Give the extent of all white blood cells.
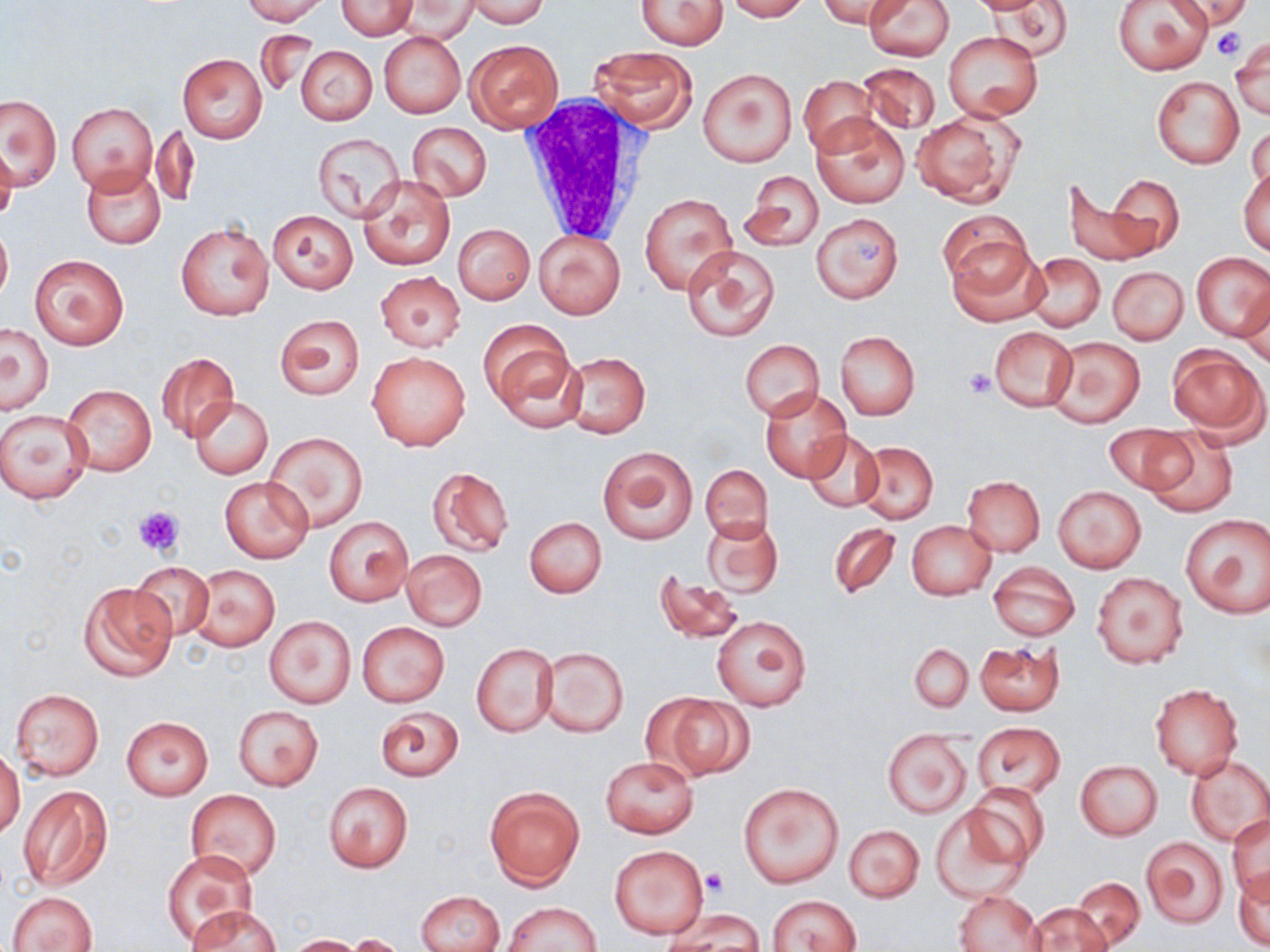

Approximate bounding boxes as named x1/y1/x2/y2 corners in pixels.
White blood cells: (x1=517, y1=93, x2=650, y2=247).

slide-level diagnosis = no evidence of blood parasites
magnification = 1000x
uninfected red blood cell locations = approximate bounding boxes as named x1/y1/x2/y2 corners in pixels: (x1=239, y1=0, x2=329, y2=24), (x1=335, y1=0, x2=417, y2=39), (x1=724, y1=0, x2=809, y2=21), (x1=819, y1=0, x2=906, y2=32), (x1=863, y1=0, x2=954, y2=60), (x1=983, y1=0, x2=1075, y2=60), (x1=1173, y1=0, x2=1250, y2=31), (x1=464, y1=1, x2=552, y2=26), (x1=636, y1=1, x2=729, y2=50), (x1=1112, y1=1, x2=1213, y2=74), (x1=395, y1=2, x2=476, y2=42), (x1=255, y1=31, x2=320, y2=94), (x1=378, y1=31, x2=465, y2=118), (x1=943, y1=31, x2=1043, y2=121), (x1=464, y1=38, x2=564, y2=133), (x1=1231, y1=38, x2=1269, y2=117), (x1=295, y1=45, x2=376, y2=125), (x1=589, y1=46, x2=699, y2=132), (x1=178, y1=53, x2=267, y2=143), (x1=857, y1=61, x2=942, y2=137), (x1=698, y1=68, x2=796, y2=165), (x1=799, y1=74, x2=877, y2=156), (x1=1151, y1=77, x2=1243, y2=168), (x1=1, y1=94, x2=62, y2=188), (x1=68, y1=101, x2=158, y2=194), (x1=911, y1=110, x2=1021, y2=205), (x1=813, y1=114, x2=910, y2=209), (x1=408, y1=122, x2=492, y2=201), (x1=1248, y1=123, x2=1269, y2=198), (x1=152, y1=124, x2=198, y2=206), (x1=312, y1=133, x2=405, y2=221), (x1=0, y1=144, x2=18, y2=228), (x1=82, y1=165, x2=165, y2=249), (x1=1239, y1=167, x2=1269, y2=255), (x1=740, y1=169, x2=823, y2=253), (x1=1107, y1=174, x2=1184, y2=256), (x1=358, y1=175, x2=455, y2=271), (x1=1064, y1=180, x2=1153, y2=267), (x1=640, y1=191, x2=737, y2=294), (x1=939, y1=211, x2=1031, y2=290), (x1=267, y1=212, x2=356, y2=292), (x1=812, y1=213, x2=903, y2=303), (x1=0, y1=223, x2=12, y2=307), (x1=176, y1=223, x2=273, y2=320), (x1=452, y1=223, x2=535, y2=305), (x1=532, y1=228, x2=626, y2=319), (x1=947, y1=238, x2=1046, y2=326), (x1=682, y1=244, x2=779, y2=342), (x1=1023, y1=252, x2=1105, y2=331), (x1=1192, y1=252, x2=1270, y2=340), (x1=31, y1=254, x2=129, y2=350), (x1=1107, y1=267, x2=1188, y2=345), (x1=375, y1=271, x2=465, y2=352), (x1=1238, y1=288, x2=1270, y2=368), (x1=274, y1=313, x2=365, y2=401), (x1=480, y1=320, x2=580, y2=427), (x1=1, y1=322, x2=54, y2=413), (x1=989, y1=326, x2=1077, y2=412), (x1=834, y1=331, x2=920, y2=420), (x1=1046, y1=335, x2=1145, y2=427), (x1=740, y1=340, x2=825, y2=420), (x1=1168, y1=346, x2=1265, y2=438), (x1=366, y1=351, x2=471, y2=451), (x1=562, y1=351, x2=650, y2=438), (x1=156, y1=353, x2=239, y2=442), (x1=63, y1=384, x2=156, y2=476), (x1=761, y1=386, x2=852, y2=482), (x1=189, y1=396, x2=273, y2=479), (x1=1, y1=408, x2=92, y2=503), (x1=1103, y1=425, x2=1189, y2=493), (x1=1141, y1=427, x2=1239, y2=517), (x1=802, y1=430, x2=885, y2=514), (x1=266, y1=433, x2=368, y2=533), (x1=855, y1=441, x2=938, y2=522), (x1=598, y1=446, x2=697, y2=545), (x1=701, y1=465, x2=772, y2=544), (x1=426, y1=466, x2=515, y2=558), (x1=220, y1=475, x2=312, y2=563), (x1=962, y1=476, x2=1045, y2=555), (x1=1053, y1=485, x2=1146, y2=573), (x1=1179, y1=514, x2=1269, y2=618), (x1=324, y1=515, x2=413, y2=607), (x1=525, y1=517, x2=606, y2=597), (x1=702, y1=517, x2=783, y2=598), (x1=907, y1=521, x2=996, y2=599), (x1=827, y1=522, x2=899, y2=600), (x1=401, y1=551, x2=487, y2=630), (x1=131, y1=563, x2=215, y2=641), (x1=988, y1=563, x2=1080, y2=640), (x1=186, y1=564, x2=279, y2=652), (x1=653, y1=572, x2=745, y2=645), (x1=1091, y1=572, x2=1188, y2=669), (x1=78, y1=582, x2=176, y2=682), (x1=264, y1=616, x2=355, y2=707), (x1=711, y1=616, x2=812, y2=711), (x1=357, y1=622, x2=449, y2=706), (x1=975, y1=639, x2=1064, y2=717), (x1=472, y1=642, x2=556, y2=737), (x1=909, y1=643, x2=973, y2=712), (x1=537, y1=647, x2=629, y2=738), (x1=1149, y1=683, x2=1243, y2=780), (x1=8, y1=687, x2=105, y2=781), (x1=648, y1=692, x2=753, y2=781), (x1=232, y1=704, x2=325, y2=791), (x1=374, y1=705, x2=465, y2=782), (x1=122, y1=716, x2=213, y2=799), (x1=974, y1=723, x2=1065, y2=799), (x1=883, y1=731, x2=972, y2=817), (x1=1, y1=745, x2=24, y2=840), (x1=601, y1=755, x2=698, y2=837), (x1=1185, y1=755, x2=1270, y2=846), (x1=1074, y1=760, x2=1163, y2=840), (x1=737, y1=780, x2=844, y2=889), (x1=323, y1=781, x2=413, y2=872), (x1=18, y1=784, x2=113, y2=890), (x1=484, y1=786, x2=585, y2=888), (x1=965, y1=786, x2=1047, y2=868), (x1=185, y1=788, x2=282, y2=882), (x1=930, y1=804, x2=1031, y2=899), (x1=1228, y1=815, x2=1270, y2=902), (x1=845, y1=824, x2=924, y2=902), (x1=1141, y1=836, x2=1229, y2=928), (x1=610, y1=844, x2=708, y2=939), (x1=162, y1=849, x2=260, y2=944), (x1=1234, y1=868, x2=1270, y2=951), (x1=1072, y1=878, x2=1145, y2=947), (x1=417, y1=889, x2=504, y2=952), (x1=955, y1=890, x2=1044, y2=952), (x1=9, y1=891, x2=97, y2=952), (x1=768, y1=895, x2=861, y2=952), (x1=501, y1=902, x2=600, y2=951), (x1=188, y1=903, x2=280, y2=951), (x1=1025, y1=903, x2=1112, y2=952), (x1=672, y1=908, x2=764, y2=951), (x1=348, y1=934, x2=410, y2=952), (x1=287, y1=935, x2=362, y2=952)
image size = 1270×952 pixels
modality = optical microscopy
field of view = one of a larger specimen
preparation = thin blood smear
platelet locations = approximate bounding boxes as named x1/y1/x2/y2 corners in pixels: (x1=1212, y1=26, x2=1243, y2=62), (x1=963, y1=368, x2=996, y2=398), (x1=133, y1=506, x2=184, y2=557), (x1=700, y1=869, x2=728, y2=897)
stain = May-Grünwald-Giemsa